State which parasite is depicted.
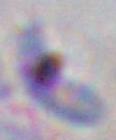

Toxoplasma gondii.

Micrograph. 1000x magnification.